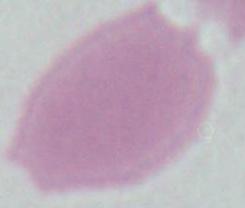

Summary:
  - Modality: micrograph
  - Magnification: 1000x
  - Identification: red blood cell